Identify the parasite.
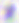
This is Toxoplasma gondii.

Captured at 400x magnification. Photomicrograph.